Assess the morphology of the erythrocytes.
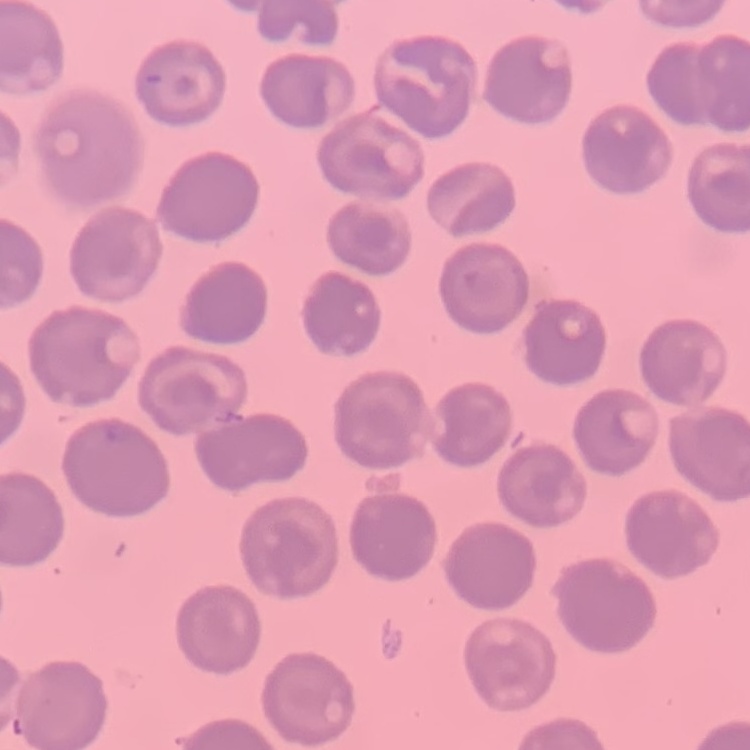
No rouleaux formation.

Square crop of a larger photomicrograph. Stained with either Field's or Giemsa. Thin peripheral smear.